Locate every uninfected red blood cell.
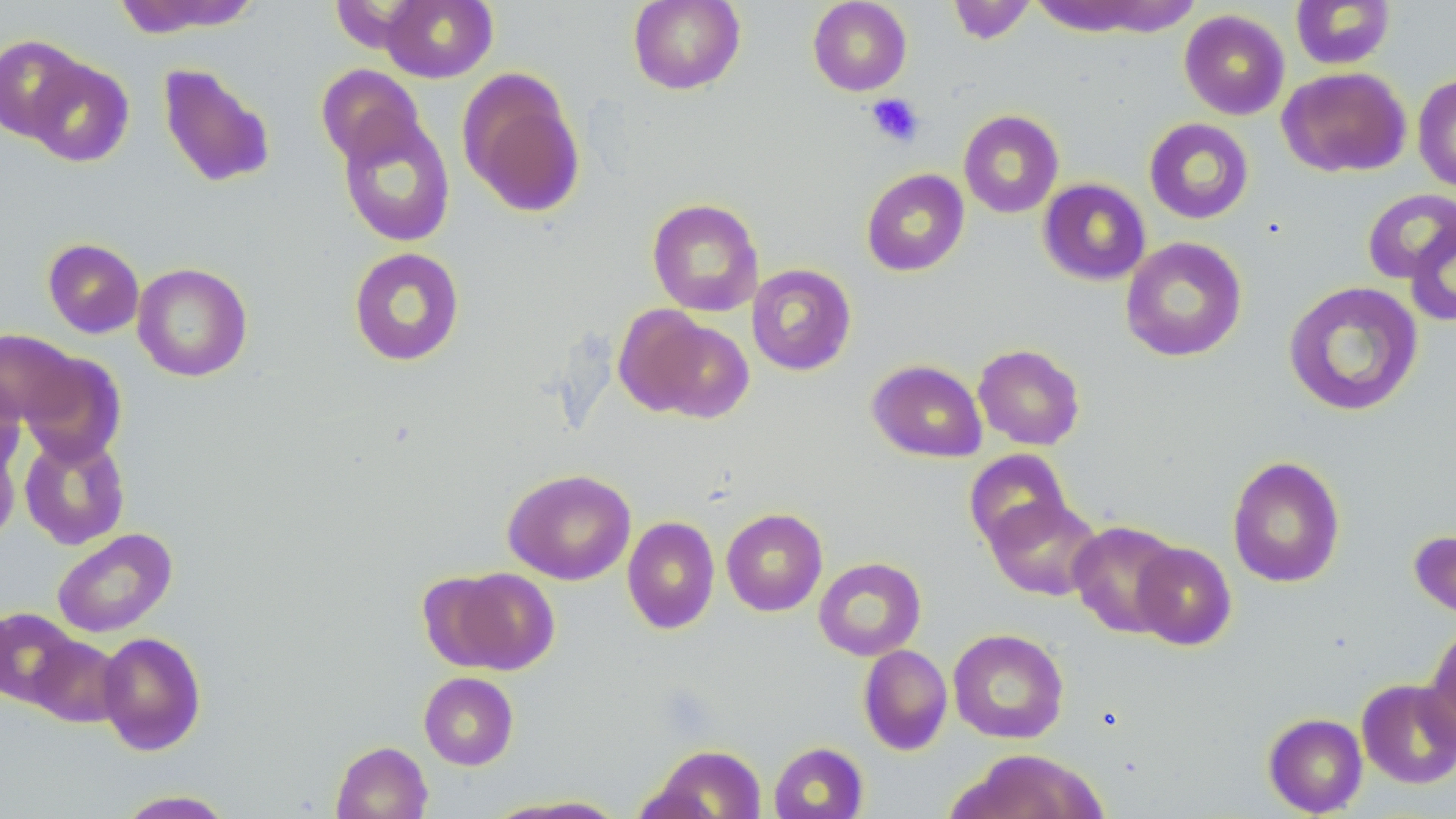
Approximate bounding boxes as (x1, y1, x2, y2) in pixels.
Uninfected red blood cells: (109, 0, 260, 37), (380, 0, 498, 83), (627, 0, 746, 95), (808, 0, 912, 96), (1290, 0, 1396, 70), (947, 1, 1037, 45), (1027, 1, 1200, 38), (1179, 10, 1290, 120), (0, 35, 89, 143), (25, 58, 134, 167), (157, 62, 277, 189), (315, 64, 425, 167), (1277, 66, 1411, 178), (457, 69, 586, 219), (1412, 74, 1456, 193), (336, 110, 456, 247), (958, 110, 1065, 218), (1144, 118, 1254, 224), (861, 168, 970, 277), (1038, 178, 1151, 285), (1362, 189, 1456, 284), (647, 197, 764, 316), (1404, 218, 1456, 326), (1120, 237, 1248, 362), (42, 238, 144, 338), (348, 246, 465, 366), (132, 263, 253, 381), (746, 264, 856, 376), (1283, 280, 1423, 417), (620, 309, 755, 423), (0, 329, 81, 427), (973, 343, 1086, 451), (20, 353, 127, 466), (867, 359, 987, 463), (0, 374, 24, 477), (19, 433, 130, 550), (0, 436, 20, 547), (963, 448, 1072, 551), (1226, 455, 1346, 588), (502, 468, 636, 585), (984, 495, 1103, 601), (721, 508, 828, 616), (622, 516, 720, 634), (1067, 520, 1184, 638), (1409, 527, 1456, 621), (51, 528, 177, 638), (1131, 542, 1237, 650), (813, 557, 927, 660), (435, 567, 560, 674), (1, 607, 81, 707), (1423, 625, 1456, 752), (948, 628, 1069, 744), (96, 631, 207, 756), (27, 634, 125, 727), (858, 644, 953, 755), (419, 671, 519, 770), (1357, 678, 1456, 789), (1263, 712, 1368, 817), (331, 741, 432, 819), (768, 741, 868, 819), (648, 744, 767, 818), (954, 749, 1109, 819), (114, 789, 237, 818), (487, 796, 630, 818).

Platelet locations: (865, 93, 924, 147). Slide-level diagnosis: negative for blood parasites. Light microscopy. Thin blood smear. May-Grünwald-Giemsa stain. One field of a larger specimen. Image is 1456×819 pixels. Captured at 1000x magnification.